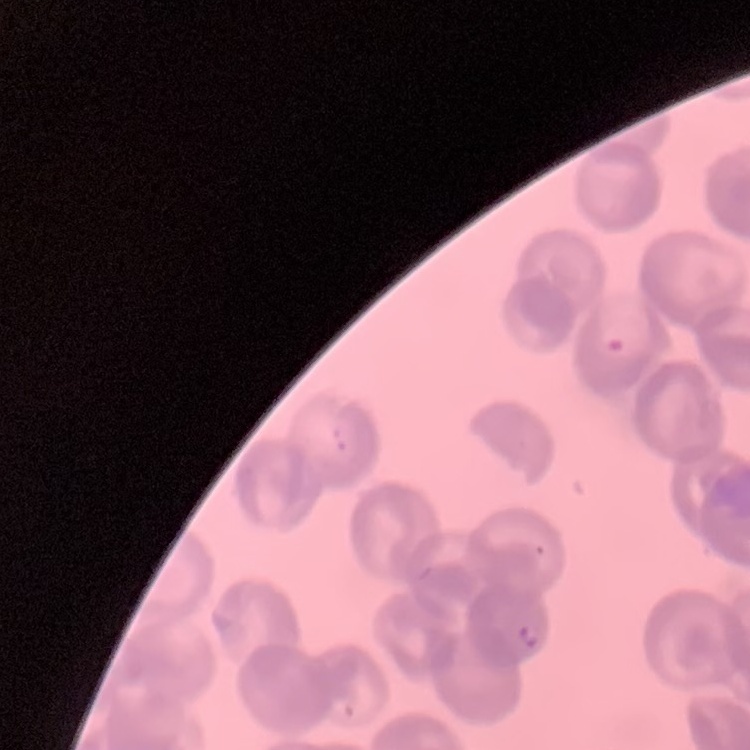

erythrocyte_morphology: rouleaux formation
preparation: thin peripheral smear
stain: Field's or Giemsa
image_type: square crop of a larger photomicrograph